State which cell type is depicted.
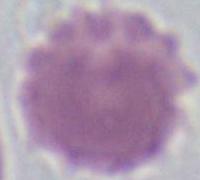

An erythrocyte.

Captured at 1000x magnification. Photomicrograph.